Report the malaria status of this cell.
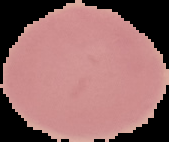

Uninfected.

Image is 169×142 pixels. The area outside the segmented cell region is set to black. From a thin blood film.